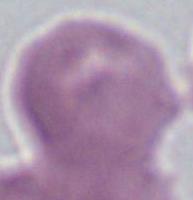
Summary:
  - Magnification: 1000x
  - Identification: erythrocyte
  - Modality: micrograph